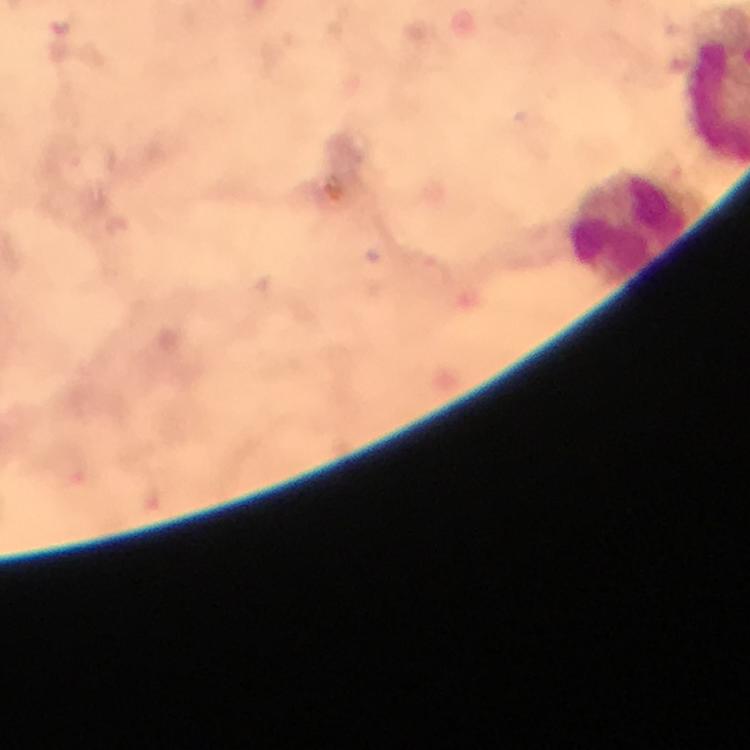
Approximate object centers, in pixels from the top-left corner.
Summary:
  - Leukocyte locations: (x=628, y=222)
  - Immersion oil: used
  - Stain: Giemsa
  - Preparation: thick blood smear
  - Image size: 750×750 pixels
  - Cropped from: a single field of view
  - Capture: smartphone camera through the microscope
  - Context: from a diagnostic examination for malaria
  - Magnification: 100x
  - Malaria parasites: none detected